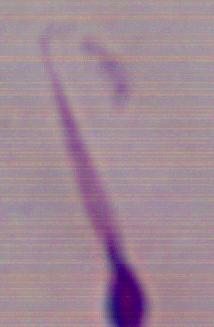
Captured at 1000x magnification. Photomicrograph. A Leishmania parasite is shown.